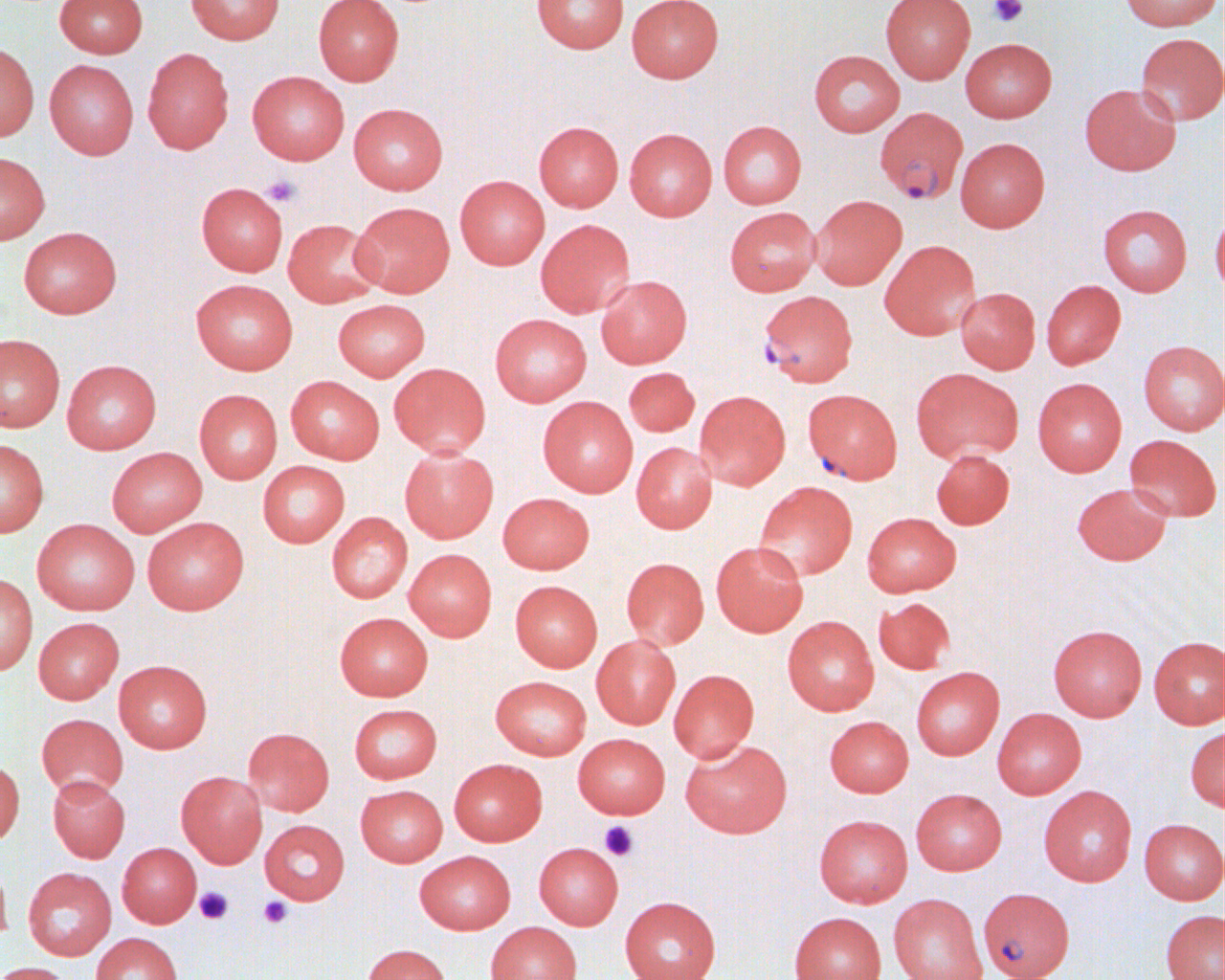
Summary:
  - Coordinate format: approximate bounding boxes as named x1/y1/x2/y2 corners in pixels
  - Uninfected red blood cell locations: (x1=54, y1=0, x2=148, y2=58), (x1=186, y1=0, x2=284, y2=44), (x1=313, y1=0, x2=404, y2=85), (x1=532, y1=0, x2=629, y2=53), (x1=626, y1=0, x2=723, y2=82), (x1=880, y1=0, x2=975, y2=84), (x1=1119, y1=0, x2=1222, y2=31), (x1=1135, y1=33, x2=1224, y2=125), (x1=960, y1=38, x2=1057, y2=122), (x1=0, y1=42, x2=39, y2=141), (x1=142, y1=47, x2=234, y2=154), (x1=808, y1=50, x2=905, y2=136), (x1=44, y1=60, x2=139, y2=159), (x1=247, y1=70, x2=349, y2=165), (x1=1079, y1=83, x2=1181, y2=175), (x1=348, y1=102, x2=448, y2=194), (x1=718, y1=120, x2=806, y2=209), (x1=534, y1=121, x2=623, y2=211), (x1=624, y1=127, x2=717, y2=221), (x1=955, y1=137, x2=1050, y2=232), (x1=0, y1=152, x2=50, y2=244), (x1=455, y1=175, x2=549, y2=270), (x1=196, y1=182, x2=288, y2=276), (x1=811, y1=195, x2=907, y2=290), (x1=350, y1=201, x2=455, y2=297), (x1=1097, y1=204, x2=1192, y2=296), (x1=724, y1=207, x2=821, y2=296), (x1=1211, y1=207, x2=1224, y2=297), (x1=283, y1=218, x2=382, y2=307), (x1=535, y1=219, x2=635, y2=318), (x1=18, y1=226, x2=122, y2=318), (x1=879, y1=240, x2=980, y2=340), (x1=596, y1=275, x2=692, y2=368), (x1=191, y1=278, x2=298, y2=374), (x1=1041, y1=280, x2=1126, y2=370), (x1=954, y1=287, x2=1041, y2=374), (x1=333, y1=299, x2=430, y2=381), (x1=490, y1=314, x2=592, y2=406), (x1=0, y1=333, x2=65, y2=432), (x1=1138, y1=340, x2=1225, y2=435), (x1=61, y1=359, x2=161, y2=454), (x1=389, y1=363, x2=490, y2=457), (x1=623, y1=367, x2=699, y2=436), (x1=911, y1=368, x2=1022, y2=463), (x1=286, y1=375, x2=384, y2=464), (x1=1032, y1=377, x2=1127, y2=477), (x1=194, y1=389, x2=283, y2=484), (x1=694, y1=390, x2=790, y2=490), (x1=538, y1=396, x2=638, y2=497), (x1=1124, y1=434, x2=1221, y2=521), (x1=0, y1=438, x2=49, y2=537), (x1=631, y1=441, x2=717, y2=533), (x1=399, y1=446, x2=498, y2=543), (x1=106, y1=447, x2=207, y2=536), (x1=931, y1=449, x2=1014, y2=529), (x1=258, y1=461, x2=350, y2=547), (x1=753, y1=481, x2=858, y2=581), (x1=1071, y1=482, x2=1172, y2=565), (x1=498, y1=492, x2=594, y2=574), (x1=327, y1=512, x2=413, y2=603), (x1=862, y1=512, x2=961, y2=596), (x1=142, y1=517, x2=248, y2=615), (x1=32, y1=519, x2=140, y2=615), (x1=711, y1=540, x2=808, y2=637), (x1=404, y1=549, x2=497, y2=641), (x1=621, y1=557, x2=709, y2=649), (x1=0, y1=573, x2=37, y2=675), (x1=510, y1=580, x2=602, y2=671), (x1=873, y1=597, x2=955, y2=674), (x1=335, y1=612, x2=433, y2=700), (x1=782, y1=616, x2=879, y2=715), (x1=33, y1=617, x2=123, y2=704), (x1=1048, y1=624, x2=1147, y2=721), (x1=591, y1=635, x2=680, y2=729), (x1=1149, y1=636, x2=1225, y2=729), (x1=113, y1=660, x2=212, y2=753), (x1=911, y1=666, x2=1004, y2=760), (x1=669, y1=669, x2=759, y2=762), (x1=490, y1=675, x2=591, y2=759), (x1=349, y1=704, x2=442, y2=783), (x1=992, y1=708, x2=1086, y2=799), (x1=36, y1=713, x2=128, y2=799), (x1=824, y1=715, x2=913, y2=797), (x1=1185, y1=726, x2=1225, y2=811), (x1=243, y1=727, x2=334, y2=816), (x1=572, y1=733, x2=670, y2=818), (x1=681, y1=739, x2=792, y2=838), (x1=449, y1=758, x2=547, y2=846), (x1=0, y1=759, x2=24, y2=846), (x1=176, y1=771, x2=267, y2=868), (x1=48, y1=775, x2=130, y2=862), (x1=355, y1=784, x2=448, y2=867), (x1=1038, y1=785, x2=1137, y2=886), (x1=910, y1=788, x2=1006, y2=875), (x1=814, y1=814, x2=912, y2=907), (x1=1139, y1=818, x2=1225, y2=904), (x1=259, y1=819, x2=349, y2=905), (x1=117, y1=842, x2=201, y2=928), (x1=534, y1=842, x2=623, y2=929), (x1=414, y1=850, x2=515, y2=934), (x1=0, y1=856, x2=12, y2=946), (x1=23, y1=867, x2=116, y2=960), (x1=888, y1=894, x2=988, y2=980), (x1=619, y1=896, x2=722, y2=980), (x1=1160, y1=909, x2=1225, y2=980), (x1=788, y1=912, x2=886, y2=980), (x1=486, y1=922, x2=582, y2=980), (x1=91, y1=932, x2=182, y2=980), (x1=361, y1=944, x2=451, y2=980), (x1=0, y1=962, x2=75, y2=980)
  - Platelet locations: (x1=989, y1=0, x2=1028, y2=27), (x1=261, y1=175, x2=301, y2=208), (x1=600, y1=821, x2=638, y2=861), (x1=195, y1=887, x2=234, y2=925), (x1=258, y1=896, x2=292, y2=929)
  - Plasmodium falciparum-infected red blood cell locations: (x1=874, y1=107, x2=969, y2=206), (x1=758, y1=290, x2=857, y2=387), (x1=802, y1=388, x2=903, y2=484), (x1=978, y1=887, x2=1074, y2=980)
  - Slide-level diagnosis: Plasmodium falciparum
  - Magnification: 1000x
  - Image size: 1225×980 pixels
  - Modality: optical microscopy
  - Field of view: single
  - Preparation: thin blood film